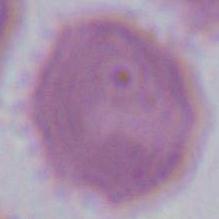
An erythrocyte is shown. Photomicrograph. Captured at 1000x magnification.